Assess the morphology of the red blood cells.
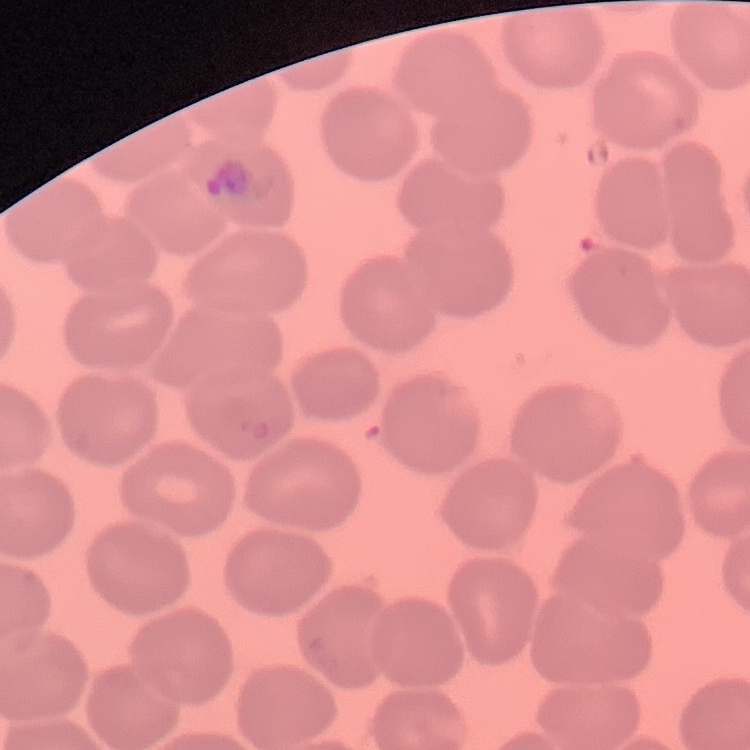
They show no rouleaux formation.

preparation = thin blood smear
image type = one tile cut from a larger photomicrograph
stain = Field's or Giemsa